Classify this cell by malaria status.
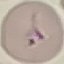
It is uninfected.

Summary:
  - Capture: smartphone through the microscope eyepiece
  - Preparation: thin blood smear
  - Image type: cell patch, automatically extracted from a larger field of view and resized to 64 × 64 pixels
  - Stain: Giemsa